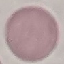
Summary:
  - Result: no malaria parasites seen
  - Capture: smartphone camera at the microscope eyepiece
  - Stain: Giemsa
  - Preparation: thin blood smear
  - Image type: automatically extracted cell patch, resized to 64 × 64 pixels